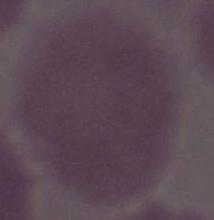 An erythrocyte is seen. Micrograph. Captured at 1000x magnification.